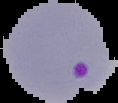

Summary:
  - Preparation: thin blood film
  - Image size: 118×103 pixels
  - Image type: segmented cell region on a black background
  - Result: malaria parasites identified